Assess this cell for malaria.
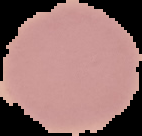
It is uninfected.

Summary:
  - Image size: 142×136 pixels
  - Image type: cell region segmented out of the field of view; surrounding area masked to black
  - Preparation: thin blood film